Classify this cell by malaria status.
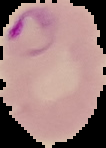
It is parasitized.

image size = 106×148 pixels
image type = segmented cell region on a black background
preparation = thin blood smear